Classify this cell by malaria status.
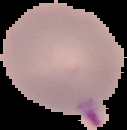

It is parasitized.

Summary:
  - Image size: 127×130 pixels
  - Image type: segmented cell region on a black background
  - Preparation: thin blood smear